Name the parasite shown.
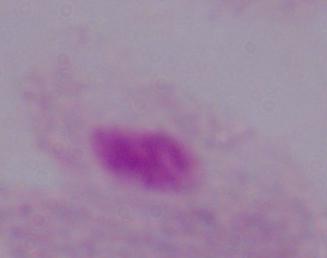

This is a trichomonad.

Summary:
  - Magnification: 1000x
  - Modality: photomicrograph